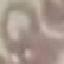

malaria status = uninfected
image type = automatically extracted cell patch, resized to 64 × 64 pixels
capture = smartphone through the microscope eyepiece
preparation = thin blood smear
stain = Giemsa